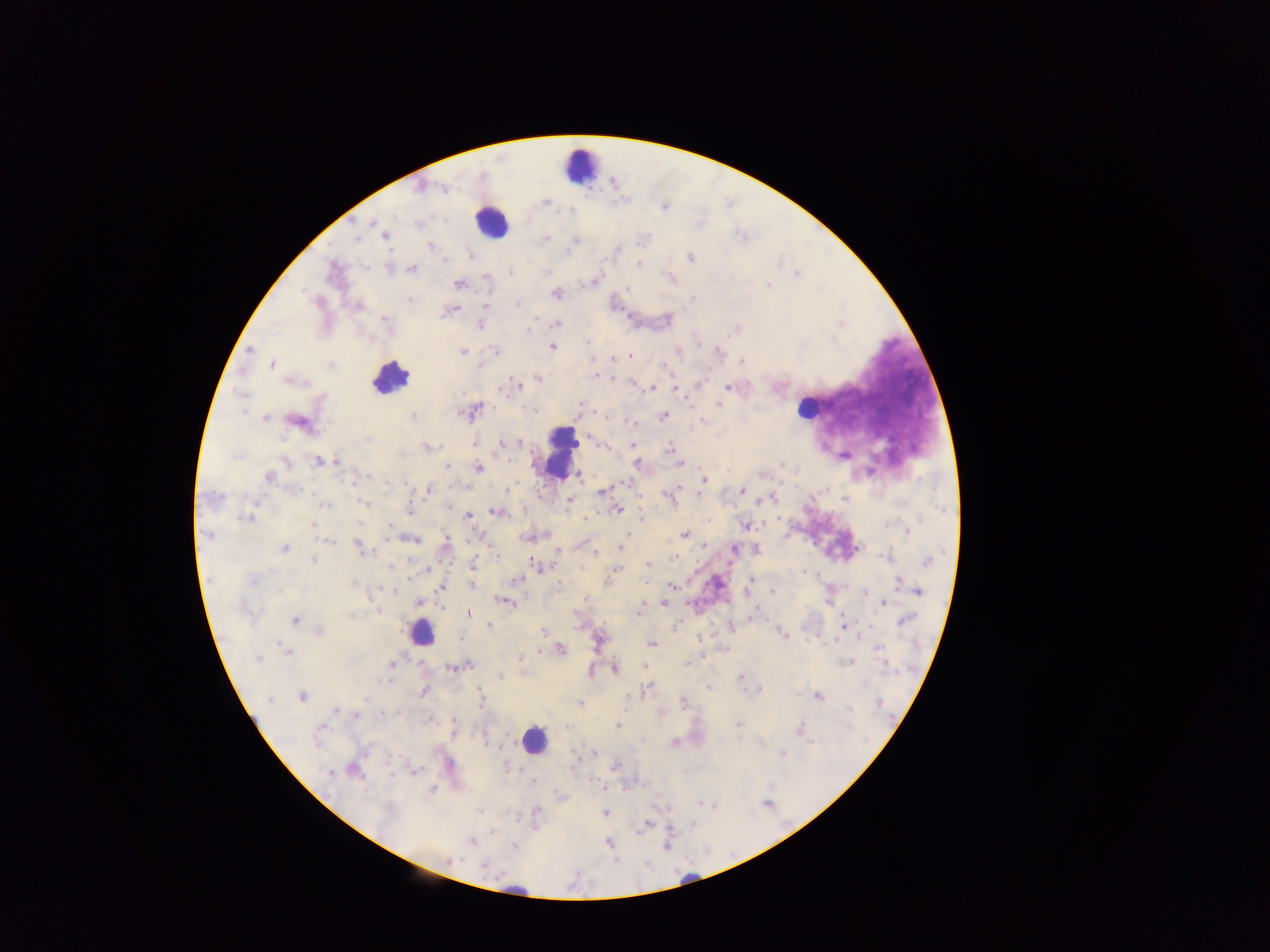

Approximate centers as {x, y} in pixels.
Summary:
  - Leukocyte locations: {579, 164}, {491, 220}, {390, 377}, {808, 407}, {558, 451}, {421, 632}, {534, 740}
  - Plasmodium parasite locations: {441, 189}, {546, 202}, {445, 221}, {371, 223}, {418, 223}, {385, 235}, {546, 238}, {357, 239}, {575, 240}, {429, 246}, {568, 251}, {471, 256}, {690, 257}, {638, 265}, {411, 269}, {510, 272}, {547, 272}, {797, 273}, {459, 285}, {768, 285}, {628, 288}, {556, 294}, {693, 299}, {319, 301}, {409, 301}, {517, 303}, {487, 304}, {357, 306}, {451, 310}, {386, 320}, {480, 324}, {556, 324}, {529, 330}, {588, 342}, {553, 347}, {250, 349}, {494, 350}, {463, 351}, {678, 351}, {718, 354}, {630, 356}, {614, 358}, {743, 362}, {272, 365}, {479, 365}, {664, 366}, {598, 375}, {538, 379}, {293, 382}, {633, 383}, {515, 384}, {728, 387}, {652, 388}, {676, 389}, {720, 404}, {475, 409}, {534, 411}, {243, 413}, {412, 415}, {664, 415}, {265, 418}, {297, 421}, {702, 421}, {631, 423}, {368, 440}, {501, 443}, {520, 443}, {429, 446}, {632, 446}, {669, 448}, {511, 461}, {286, 462}, {318, 462}, {336, 462}, {680, 463}, {637, 464}, {446, 466}, {478, 468}, {269, 476}, {580, 476}, {703, 479}, {352, 481}, {427, 490}, {741, 491}, {601, 492}, {699, 493}, {214, 495}, {773, 497}, {670, 498}, {569, 500}, {364, 503}, {325, 506}, {449, 508}, {410, 509}, {618, 509}, {496, 512}, {467, 515}, {247, 518}, {585, 518}, {641, 519}, {312, 525}, {745, 525}, {389, 527}, {907, 531}, {206, 535}, {684, 535}, {625, 537}, {414, 540}, {329, 541}, {446, 543}, {358, 546}, {704, 546}, {285, 548}, {620, 548}, {733, 549}, {556, 551}, {757, 551}, {595, 554}, {495, 555}, {676, 557}, {886, 557}, {313, 561}, {533, 561}, {927, 561}, {647, 564}, {473, 566}, {391, 568}, {427, 569}, {614, 571}, {805, 572}, {410, 577}, {516, 579}, {253, 580}, {751, 581}, {898, 583}, {471, 584}, {352, 585}, {672, 586}, {442, 588}, {388, 589}, {919, 591}, {773, 592}, {865, 592}, {585, 599}, {503, 602}, {419, 603}, {663, 604}, {883, 604}, {638, 610}, {377, 611}, {468, 613}, {756, 613}, {294, 620}, {906, 620}, {489, 626}, {843, 627}, {320, 631}, {543, 632}, {782, 634}, {651, 644}, {879, 647}, {561, 649}, {286, 652}, {258, 658}, {520, 658}, {848, 663}, {391, 665}, {688, 665}, {453, 668}, {615, 669}, {591, 672}, {500, 676}, {740, 677}, {709, 686}, {648, 688}, {759, 690}, {423, 692}, {819, 696}, {302, 697}, {364, 699}, {481, 699}, {269, 700}, {683, 702}, {879, 702}, {580, 703}, {337, 710}, {849, 710}, {396, 712}, {390, 713}, {356, 715}, {454, 724}, {738, 724}, {617, 727}, {321, 728}, {800, 729}, {812, 743}, {674, 744}, {782, 753}, {390, 761}, {617, 766}, {508, 769}, {355, 771}, {330, 772}, {432, 790}, {701, 803}, {389, 809}, {480, 811}, {605, 813}, {646, 824}, {694, 825}, {493, 832}, {472, 841}, {609, 844}, {514, 846}, {450, 860}, {485, 866}
  - Capture: mobile-phone photograph through a microscope
  - Preparation: thick blood film
  - Image size: 1270×952 pixels
  - Field of view: single
  - Country: Ghana